Outline each Plasmodium falciparum-infected red blood cell.
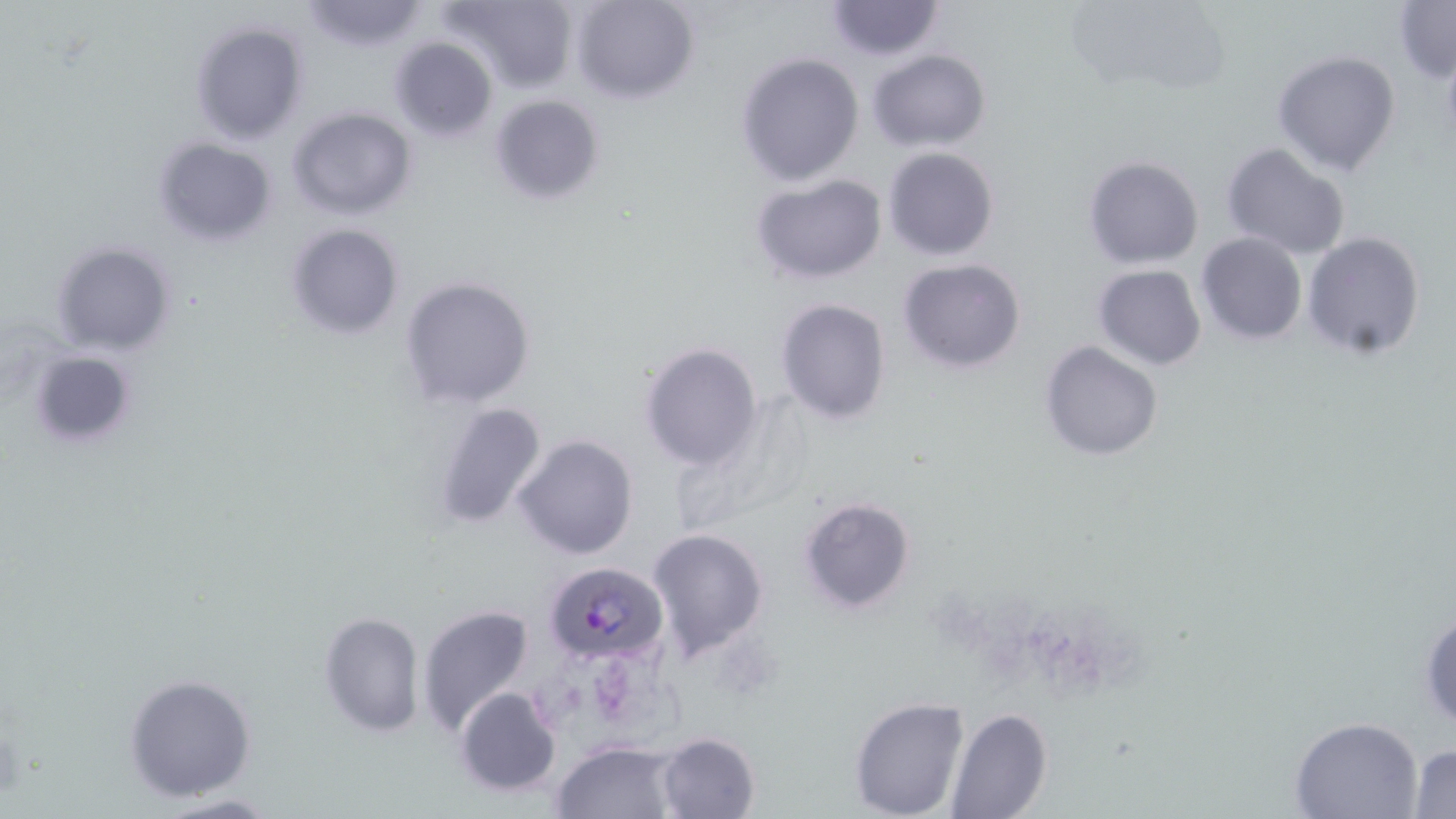
Approximate bounding boxes as named x1/y1/x2/y2 corners in pixels.
Plasmodium falciparum-infected red blood cells: (x1=544, y1=561, x2=668, y2=667).

Uninfected red blood cell locations: (x1=298, y1=0, x2=431, y2=51), (x1=441, y1=0, x2=579, y2=92), (x1=570, y1=0, x2=700, y2=105), (x1=1080, y1=0, x2=1233, y2=98), (x1=823, y1=1, x2=946, y2=61), (x1=1395, y1=1, x2=1455, y2=82), (x1=189, y1=18, x2=309, y2=146), (x1=389, y1=36, x2=498, y2=143), (x1=867, y1=48, x2=991, y2=153), (x1=1272, y1=49, x2=1400, y2=177), (x1=733, y1=52, x2=866, y2=187), (x1=489, y1=94, x2=605, y2=206), (x1=286, y1=107, x2=417, y2=221), (x1=151, y1=137, x2=277, y2=247), (x1=1221, y1=143, x2=1352, y2=261), (x1=883, y1=146, x2=998, y2=260), (x1=1083, y1=156, x2=1204, y2=270), (x1=749, y1=173, x2=888, y2=285), (x1=285, y1=222, x2=404, y2=342), (x1=1302, y1=230, x2=1427, y2=359), (x1=1197, y1=232, x2=1306, y2=345), (x1=49, y1=239, x2=178, y2=357), (x1=897, y1=258, x2=1026, y2=374), (x1=1093, y1=264, x2=1206, y2=371), (x1=398, y1=274, x2=535, y2=409), (x1=775, y1=298, x2=890, y2=426), (x1=1038, y1=340, x2=1163, y2=460), (x1=639, y1=342, x2=765, y2=470), (x1=27, y1=347, x2=142, y2=453), (x1=432, y1=400, x2=551, y2=529), (x1=512, y1=434, x2=638, y2=559), (x1=797, y1=495, x2=917, y2=615), (x1=647, y1=527, x2=769, y2=660), (x1=1418, y1=600, x2=1456, y2=733), (x1=416, y1=603, x2=538, y2=741), (x1=319, y1=611, x2=425, y2=736), (x1=121, y1=672, x2=259, y2=804), (x1=454, y1=687, x2=562, y2=797), (x1=848, y1=697, x2=970, y2=818), (x1=944, y1=708, x2=1051, y2=819), (x1=1289, y1=717, x2=1424, y2=819), (x1=655, y1=731, x2=761, y2=818), (x1=552, y1=740, x2=683, y2=818), (x1=1407, y1=743, x2=1456, y2=818), (x1=145, y1=793, x2=283, y2=818). Slide-level diagnosis: Plasmodium falciparum. One field of a larger specimen. Image is 1456×819 pixels. Thin blood film. 1000x magnification. Optical microscopy. May-Grünwald-Giemsa-stained preparation.